Give the position of every malaria parasite and every leukocyte.
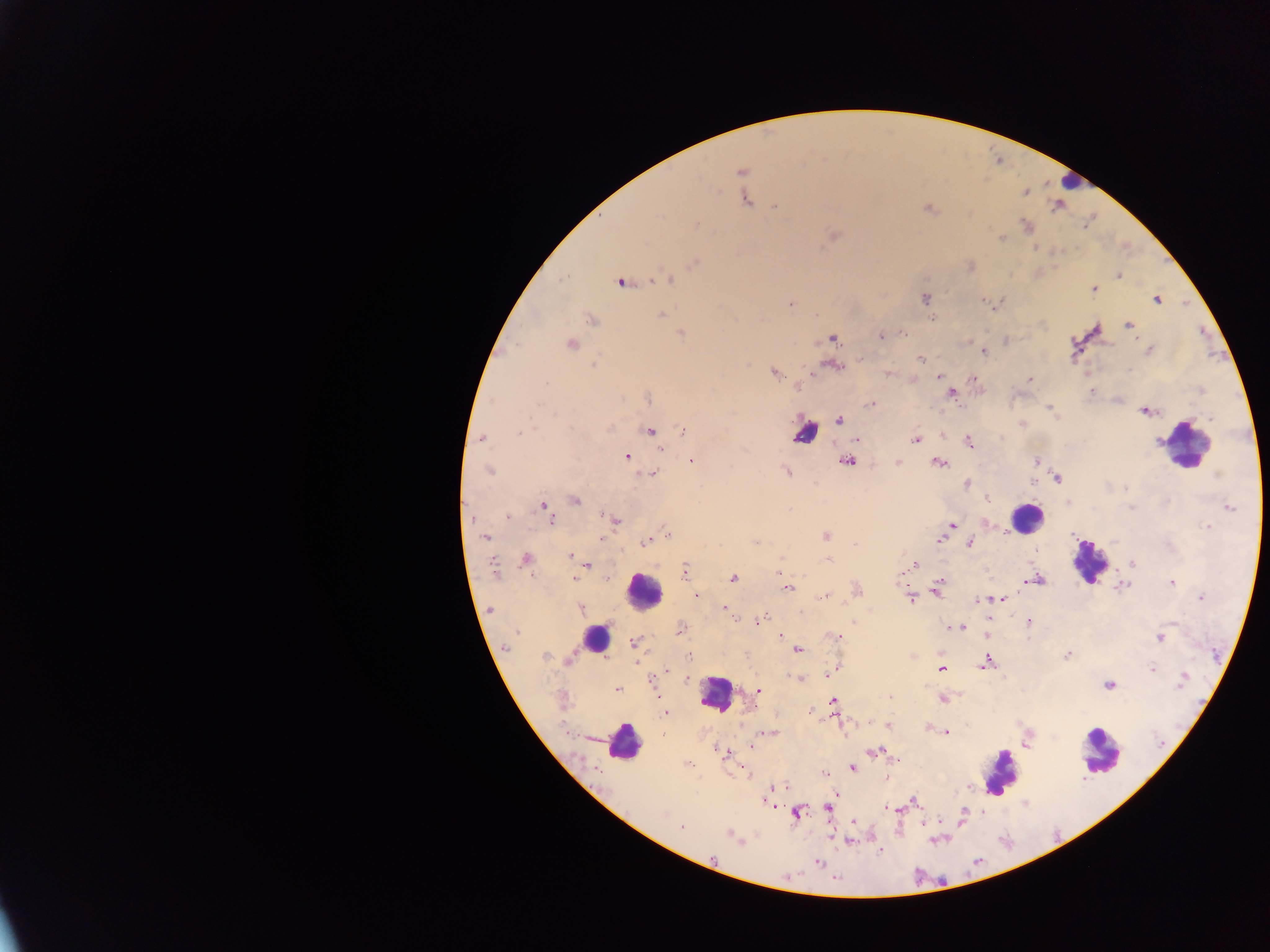

Approximate centers as {x, y} in pixels.
Malaria parasites: {741, 172}, {1026, 193}, {746, 199}, {776, 206}, {929, 209}, {697, 224}, {1026, 226}, {834, 236}, {1002, 238}, {695, 262}, {1119, 275}, {668, 279}, {621, 283}, {1094, 289}, {925, 298}, {1156, 299}, {983, 301}, {790, 303}, {661, 314}, {592, 320}, {1128, 325}, {681, 333}, {902, 333}, {880, 335}, {832, 339}, {571, 345}, {984, 351}, {1149, 351}, {920, 359}, {593, 365}, {834, 367}, {774, 373}, {888, 373}, {939, 376}, {973, 379}, {1029, 379}, {546, 383}, {798, 387}, {1091, 391}, {951, 392}, {649, 398}, {540, 404}, {870, 404}, {1049, 409}, {1145, 412}, {1210, 418}, {839, 420}, {609, 428}, {683, 430}, {650, 431}, {519, 434}, {482, 438}, {916, 439}, {856, 440}, {968, 442}, {661, 450}, {627, 456}, {692, 461}, {846, 462}, {898, 462}, {1037, 462}, {938, 463}, {489, 471}, {786, 471}, {654, 474}, {1217, 475}, {1058, 479}, {1033, 482}, {967, 484}, {1125, 489}, {575, 500}, {1069, 504}, {544, 507}, {1131, 508}, {1229, 508}, {508, 517}, {549, 519}, {613, 520}, {951, 525}, {1208, 527}, {667, 535}, {826, 536}, {485, 537}, {601, 539}, {939, 539}, {646, 541}, {756, 541}, {970, 543}, {854, 544}, {569, 556}, {526, 560}, {828, 561}, {1132, 563}, {914, 564}, {587, 565}, {493, 568}, {684, 570}, {780, 573}, {574, 578}, {605, 578}, {733, 578}, {1036, 580}, {1171, 582}, {939, 584}, {789, 587}, {1122, 587}, {858, 590}, {937, 591}, {697, 595}, {824, 596}, {1202, 597}, {911, 598}, {1004, 599}, {979, 600}, {724, 608}, {580, 609}, {490, 610}, {734, 617}, {760, 620}, {1030, 621}, {952, 627}, {962, 627}, {680, 629}, {517, 633}, {780, 636}, {835, 636}, {1160, 638}, {634, 643}, {507, 648}, {797, 650}, {1067, 655}, {544, 657}, {689, 657}, {569, 659}, {987, 662}, {1152, 668}, {835, 669}, {941, 669}, {667, 671}, {830, 673}, {798, 679}, {1182, 681}, {1109, 685}, {617, 689}, {759, 690}, {942, 699}, {833, 703}, {664, 712}, {888, 726}, {946, 732}, {769, 733}, {1027, 744}, {752, 745}, {873, 752}, {725, 753}, {687, 764}, {852, 767}, {824, 773}, {887, 778}, {781, 786}, {765, 800}, {914, 802}, {829, 808}, {887, 808}, {663, 813}, {797, 814}, {963, 815}, {853, 822}, {682, 827}, {731, 834}, {849, 840}, {879, 851}, {818, 863}.
Leukocytes: {1070, 181}, {804, 433}, {1185, 445}, {1026, 518}, {1089, 562}, {644, 591}, {595, 639}, {716, 693}, {624, 742}, {1100, 750}, {997, 773}.

Collected in Ghana. Thick blood smear. Mobile-phone photograph taken through the microscope. Image is 1270×952 pixels. Single field of view.